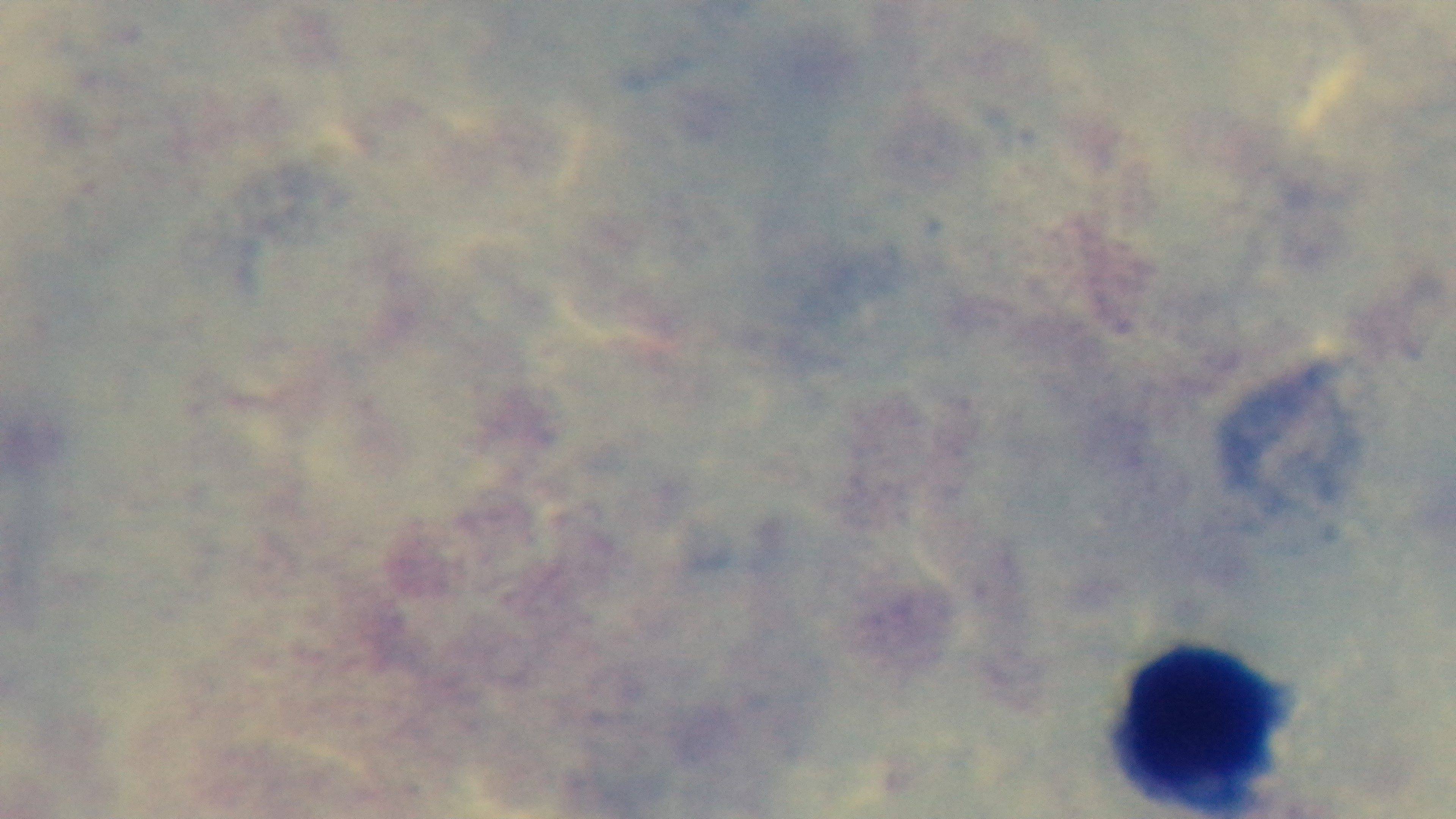

Summary:
  - Stain: Giemsa
  - Malaria status: uninfected
  - Preparation: thick blood film
  - Capture: mounted 4K digital camera
  - Field of view: one from the slide
  - Modality: light microscopy
  - Objective: 100x oil immersion